Assess this cell for malaria.
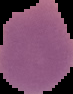

Parasitized.

preparation = thin blood film
image size = 73×94 pixels
image type = segmented cell region with the area outside set to black